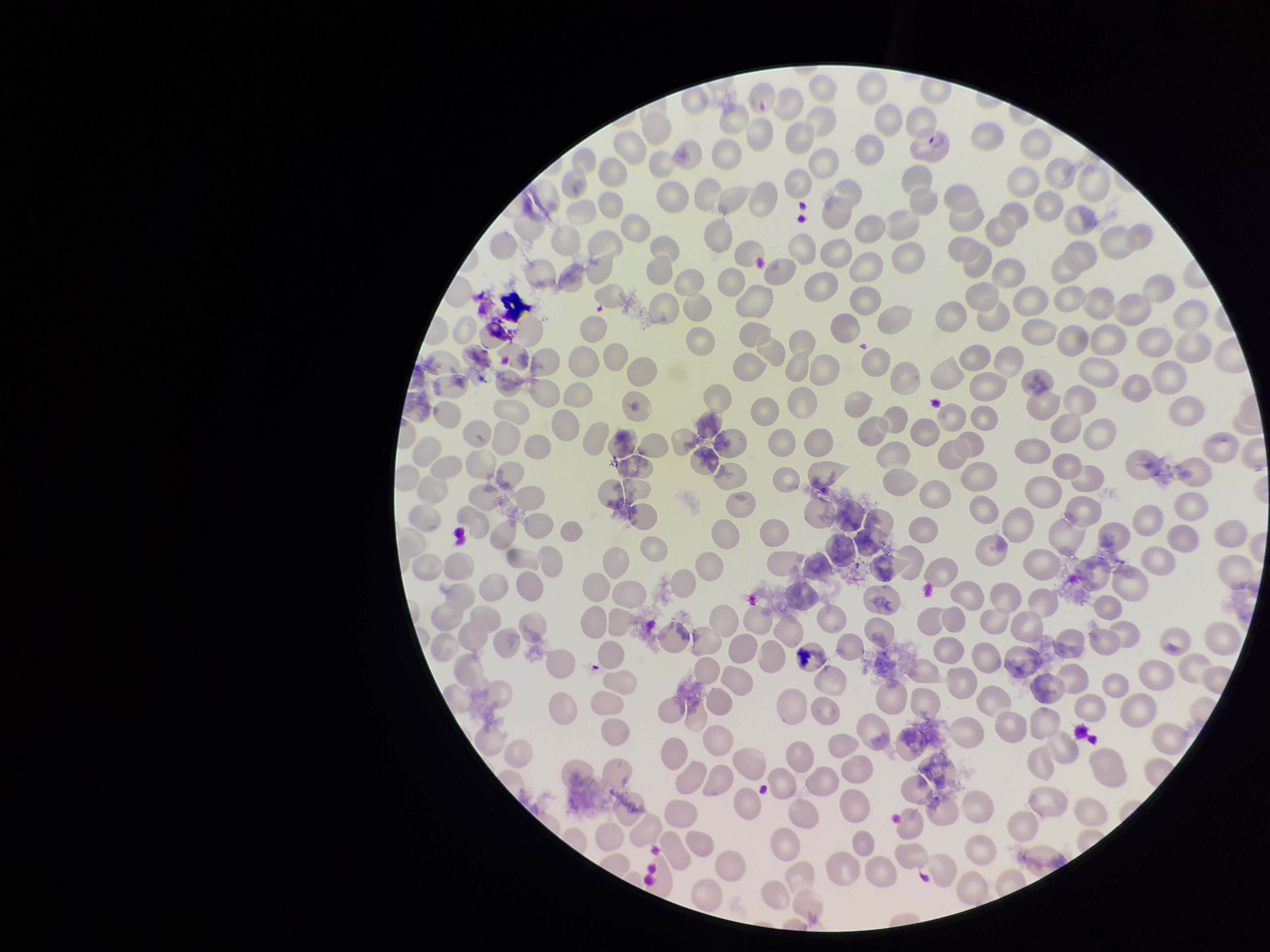

patient malaria status = positive
parasitized red blood cells = none identified
image size = 1270×952 pixels
parasitized red blood cell count = 0
species reported for this patient = Plasmodium vivax
stain = Giemsa
capture = smartphone photograph through the microscope eyepiece
red blood cell count = 307
preparation = thin
field of view = single